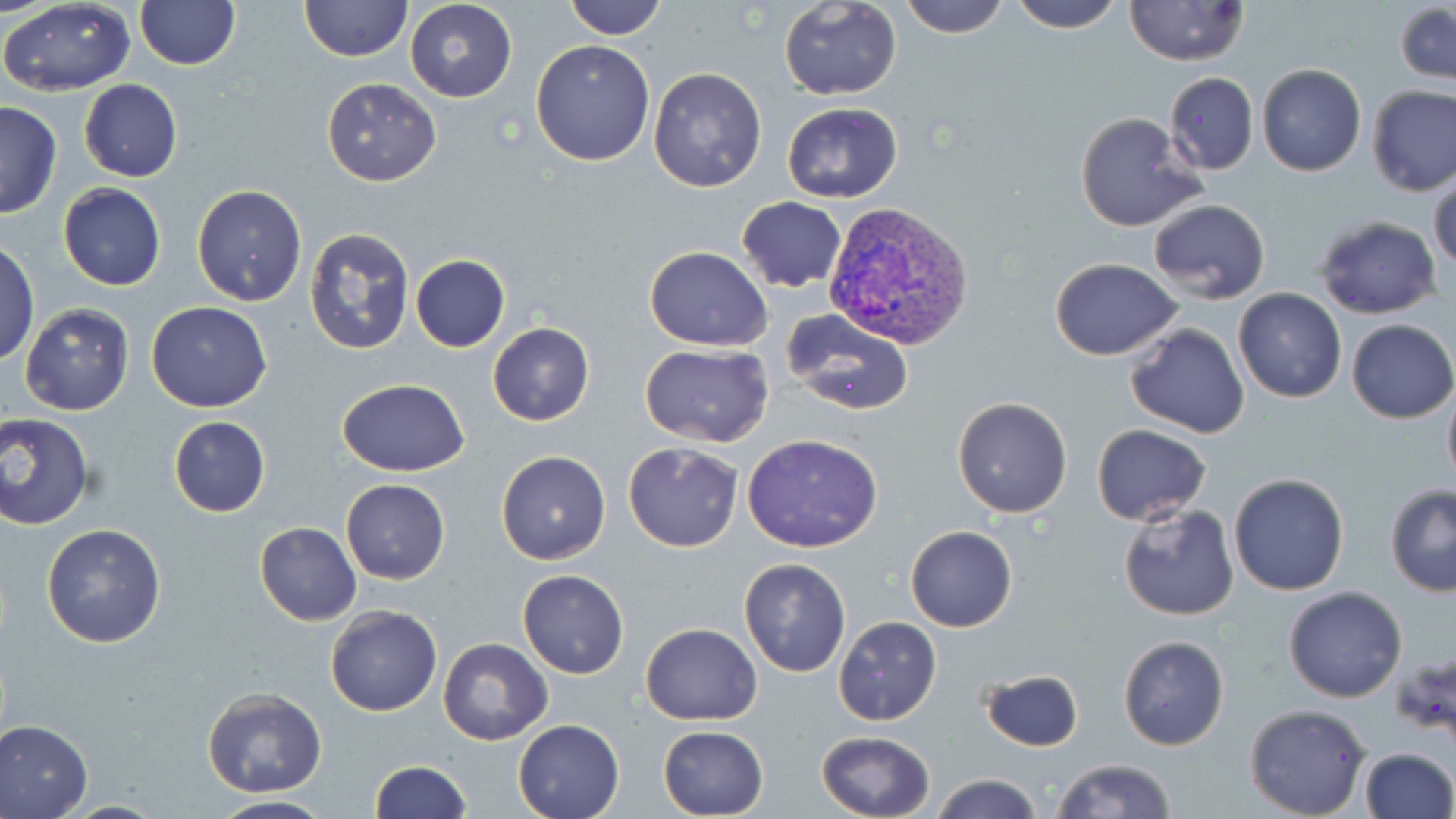
Approximate bounding boxes as (x1, y1, x2, y2) in pixels. Plasmodium vivax-infected red blood cell locations: (820, 201, 975, 352). Uninfected red blood cell locations: (563, 0, 669, 39), (780, 0, 903, 100), (898, 0, 1011, 39), (1005, 0, 1125, 33), (1125, 0, 1247, 66), (0, 1, 137, 95), (134, 1, 241, 71), (300, 1, 412, 63), (404, 1, 518, 102), (1394, 3, 1456, 85), (530, 40, 655, 167), (1258, 64, 1366, 177), (647, 66, 767, 192), (1164, 71, 1260, 175), (322, 77, 441, 185), (79, 80, 182, 182), (1365, 85, 1456, 196), (0, 102, 62, 219), (782, 102, 904, 202), (1074, 111, 1205, 233), (1429, 172, 1455, 277), (58, 183, 167, 291), (191, 183, 308, 307), (737, 196, 846, 293), (1148, 199, 1271, 303), (1315, 216, 1441, 319), (302, 226, 416, 359), (0, 242, 39, 365), (645, 246, 773, 350), (410, 254, 510, 351), (1049, 258, 1183, 360), (1234, 289, 1346, 402), (146, 301, 273, 412), (20, 302, 134, 416), (781, 309, 918, 417), (1346, 320, 1456, 424), (488, 322, 595, 426), (1125, 323, 1250, 438), (640, 344, 773, 448), (335, 377, 470, 476), (1442, 379, 1456, 490), (952, 396, 1074, 518), (0, 413, 95, 530), (168, 416, 270, 517), (1091, 423, 1213, 527), (742, 434, 882, 553), (623, 441, 743, 552), (495, 450, 611, 564), (1227, 472, 1350, 595), (340, 479, 451, 584), (1384, 485, 1456, 596), (1117, 503, 1238, 620), (255, 521, 362, 625), (41, 523, 167, 648), (906, 525, 1017, 633), (738, 558, 851, 677), (518, 569, 629, 678), (1283, 586, 1407, 702), (325, 605, 442, 717), (835, 616, 941, 725), (640, 622, 762, 726), (1118, 635, 1229, 751), (438, 636, 553, 746), (978, 669, 1084, 751), (201, 685, 327, 797), (1243, 703, 1371, 819), (0, 718, 95, 818), (513, 719, 625, 819), (658, 725, 769, 817), (815, 730, 935, 819), (1358, 748, 1454, 819), (1049, 758, 1177, 819), (368, 759, 470, 818), (931, 775, 1044, 819), (204, 794, 337, 819), (63, 799, 170, 818). Slide-level diagnosis: Plasmodium vivax. Single field of view. Light microscopy. Thin blood smear. Image is 1456×819 pixels. May-Grünwald-Giemsa-stained preparation. 1000x magnification.